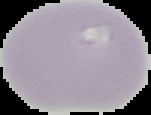

Summary:
  - Image size: 151×115 pixels
  - Malaria status: uninfected
  - Preparation: thin blood film
  - Image type: cell region segmented out of the field of view; surrounding area masked to black